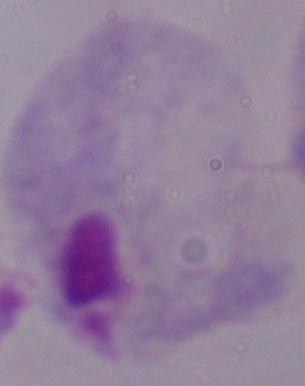
{
  "identification": "trichomonad",
  "magnification": "1000x",
  "modality": "photomicrograph"
}